Assess the morphology of the erythrocytes.
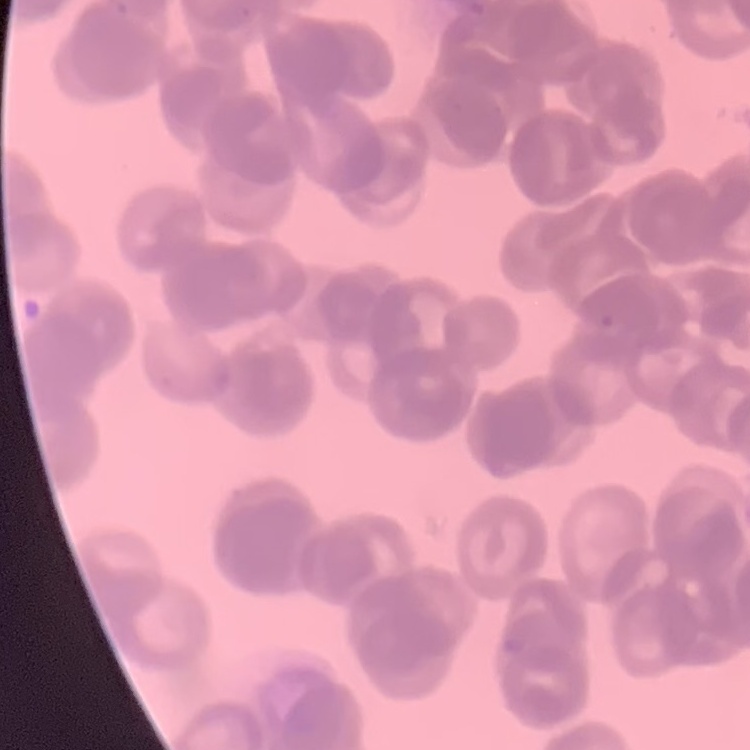
Rouleaux formation.

Summary:
  - Preparation: thin blood film
  - Image type: one tile cut from a larger photomicrograph
  - Stain: Field's or Giemsa